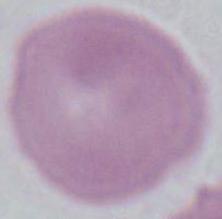

Summary:
  - Magnification: 1000x
  - Modality: micrograph
  - Identification: red blood cell